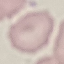
Malaria status: uninfected. Thin blood film. Acquired by smartphone through the microscope eyepiece. Giemsa-stained preparation. Cell patch, automatically extracted from a larger field of view and resized to 64 × 64 pixels.